Locate platelets.
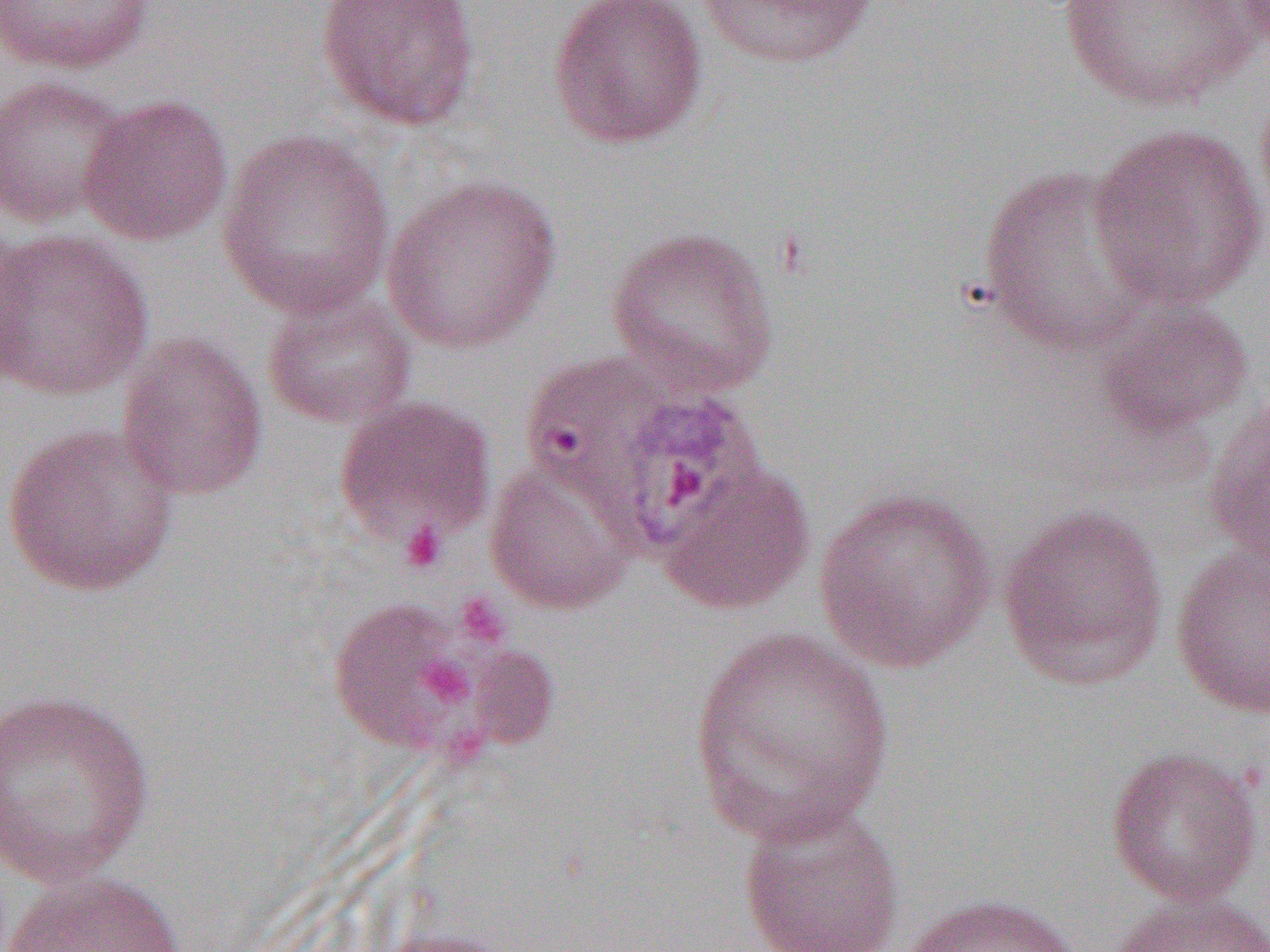

Approximate bounding boxes as (x1, y1, x2, y2) in pixels.
Platelets: (400, 521, 447, 573), (454, 594, 511, 649), (419, 657, 474, 706).

Summary:
  - Uninfected red blood cell locations: (315, 0, 483, 132), (547, 0, 708, 149), (1052, 0, 1264, 113), (1, 1, 157, 75), (693, 1, 882, 71), (1227, 1, 1270, 56), (1254, 73, 1270, 228), (0, 74, 135, 229), (77, 93, 233, 246), (1089, 122, 1269, 311), (216, 129, 395, 320), (974, 163, 1157, 354), (380, 174, 563, 355), (605, 225, 780, 397), (0, 228, 154, 401), (262, 290, 417, 429), (1093, 298, 1255, 440), (116, 332, 269, 501), (518, 349, 699, 520), (1203, 393, 1270, 570), (334, 395, 497, 548), (1, 422, 180, 597), (482, 457, 639, 616), (658, 461, 815, 616), (813, 486, 997, 673), (998, 501, 1170, 691), (1171, 540, 1270, 721), (326, 599, 484, 757), (685, 626, 896, 844), (0, 687, 156, 888), (1105, 746, 1264, 906), (736, 800, 906, 952), (1, 870, 187, 952), (1110, 892, 1270, 952), (898, 893, 1079, 952)
  - Slide-level diagnosis: Plasmodium vivax
  - Field of view: one of a larger specimen
  - Magnification: 1000x
  - Modality: light microscopy
  - Preparation: thin blood film
  - Image size: 1270×952 pixels